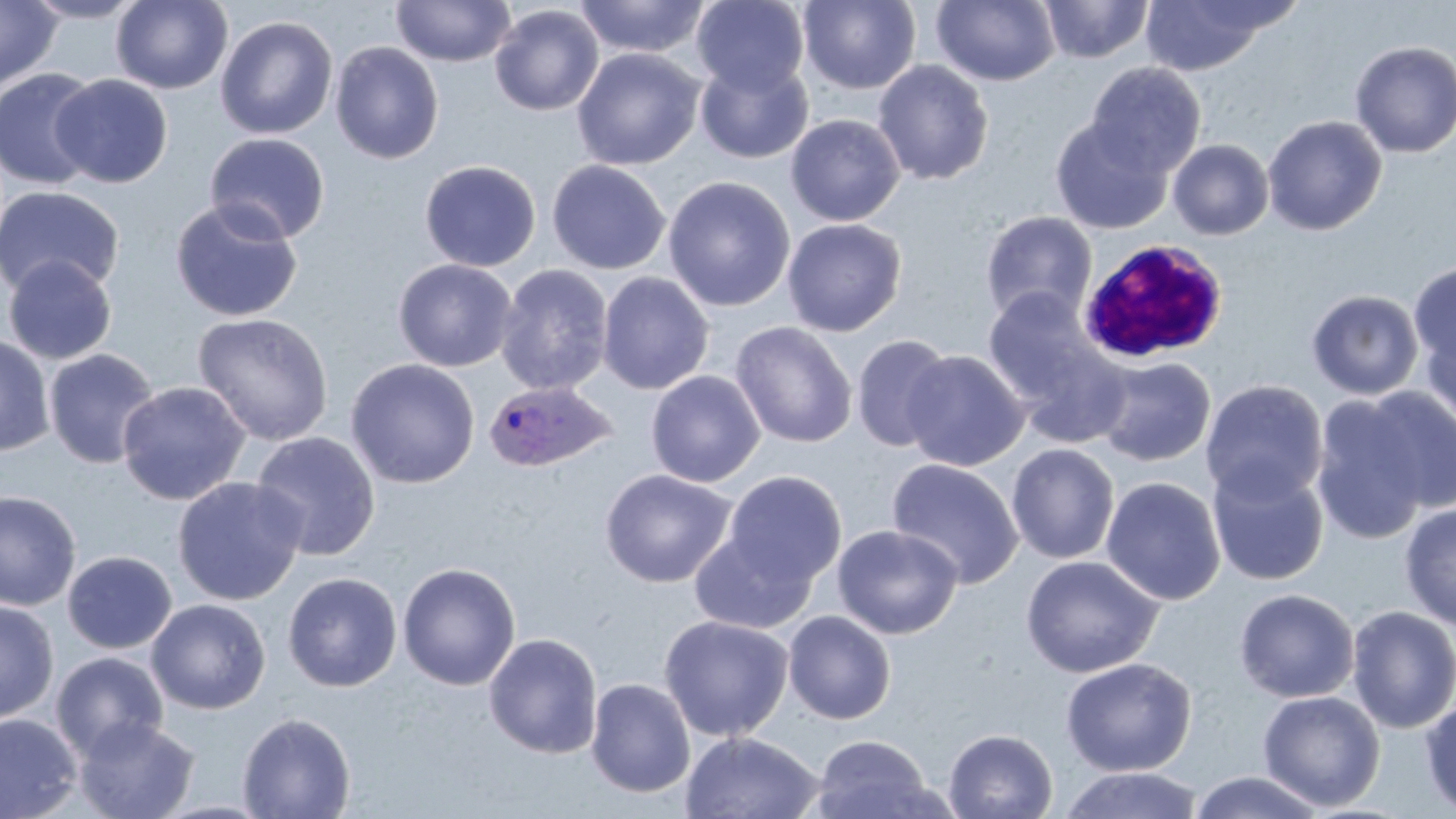
slide_level_diagnosis: Plasmodium ovale
modality: optical microscopy
field_of_view: one of a larger specimen
white_blood_cell_locations: 'approximate bounding boxes as [x1, y1, x2, y2] in pixels: [1076, 240, 1230, 366]'
image_size: 1456×819 pixels
uninfected_red_blood_cell_locations: 'approximate bounding boxes as [x1, y1, x2, y2] in pixels: [0, 0, 62, 94], [21, 0, 147, 23], [110, 0, 233, 94], [391, 0, 516, 67], [572, 0, 712, 59], [798, 0, 922, 94], [931, 0, 1061, 86], [1040, 0, 1154, 62], [1138, 0, 1278, 75], [691, 1, 810, 95], [489, 4, 604, 116], [214, 15, 338, 140], [1349, 40, 1456, 158], [330, 41, 444, 164], [572, 47, 705, 171], [696, 59, 812, 164], [872, 60, 994, 186], [1085, 61, 1206, 176], [0, 68, 102, 191], [51, 74, 173, 188], [785, 114, 905, 226], [1262, 114, 1387, 236], [1050, 118, 1173, 235], [205, 132, 331, 245], [1168, 138, 1274, 240], [419, 159, 541, 272], [546, 159, 671, 275], [663, 175, 796, 311], [0, 186, 125, 300], [170, 198, 303, 322], [980, 210, 1099, 324], [782, 218, 907, 337], [3, 255, 118, 365], [393, 258, 517, 372], [1408, 260, 1456, 374], [494, 263, 614, 397], [597, 271, 714, 395], [982, 288, 1108, 409], [1306, 289, 1424, 400], [192, 312, 334, 445], [1419, 316, 1456, 432], [730, 321, 857, 448], [0, 334, 55, 456], [850, 334, 955, 452], [43, 348, 160, 470], [902, 350, 1029, 471], [1095, 356, 1216, 466], [345, 358, 480, 489], [645, 370, 765, 487], [1200, 379, 1328, 504], [116, 380, 251, 505], [1356, 384, 1456, 517], [1310, 390, 1436, 544], [250, 431, 381, 561], [1006, 442, 1120, 564], [886, 457, 1024, 589], [1206, 462, 1329, 586], [600, 469, 737, 588], [723, 471, 846, 587], [172, 476, 307, 606], [1101, 476, 1226, 605], [0, 490, 82, 611], [1400, 503, 1456, 632], [831, 524, 963, 639], [689, 528, 816, 635], [62, 550, 177, 654], [1020, 554, 1164, 678], [397, 562, 521, 691], [282, 572, 402, 692], [1234, 588, 1359, 703], [146, 598, 271, 715], [0, 601, 59, 724], [1346, 604, 1456, 734], [783, 610, 896, 725], [658, 615, 795, 741], [484, 633, 603, 758], [51, 651, 169, 762], [1060, 657, 1198, 777], [585, 678, 696, 798], [1257, 690, 1386, 811], [1420, 697, 1456, 816], [237, 712, 356, 818], [0, 713, 82, 819], [73, 716, 200, 819], [944, 728, 1059, 819], [680, 731, 825, 818], [809, 734, 937, 819], [1058, 766, 1205, 819], [1187, 770, 1328, 819]'
stain: May-Grünwald-Giemsa
preparation: thin blood film
plasmodium_ovale_infected_red_blood_cell_locations: 'approximate bounding boxes as [x1, y1, x2, y2] in pixels: [483, 380, 617, 474]'
magnification: 1000x